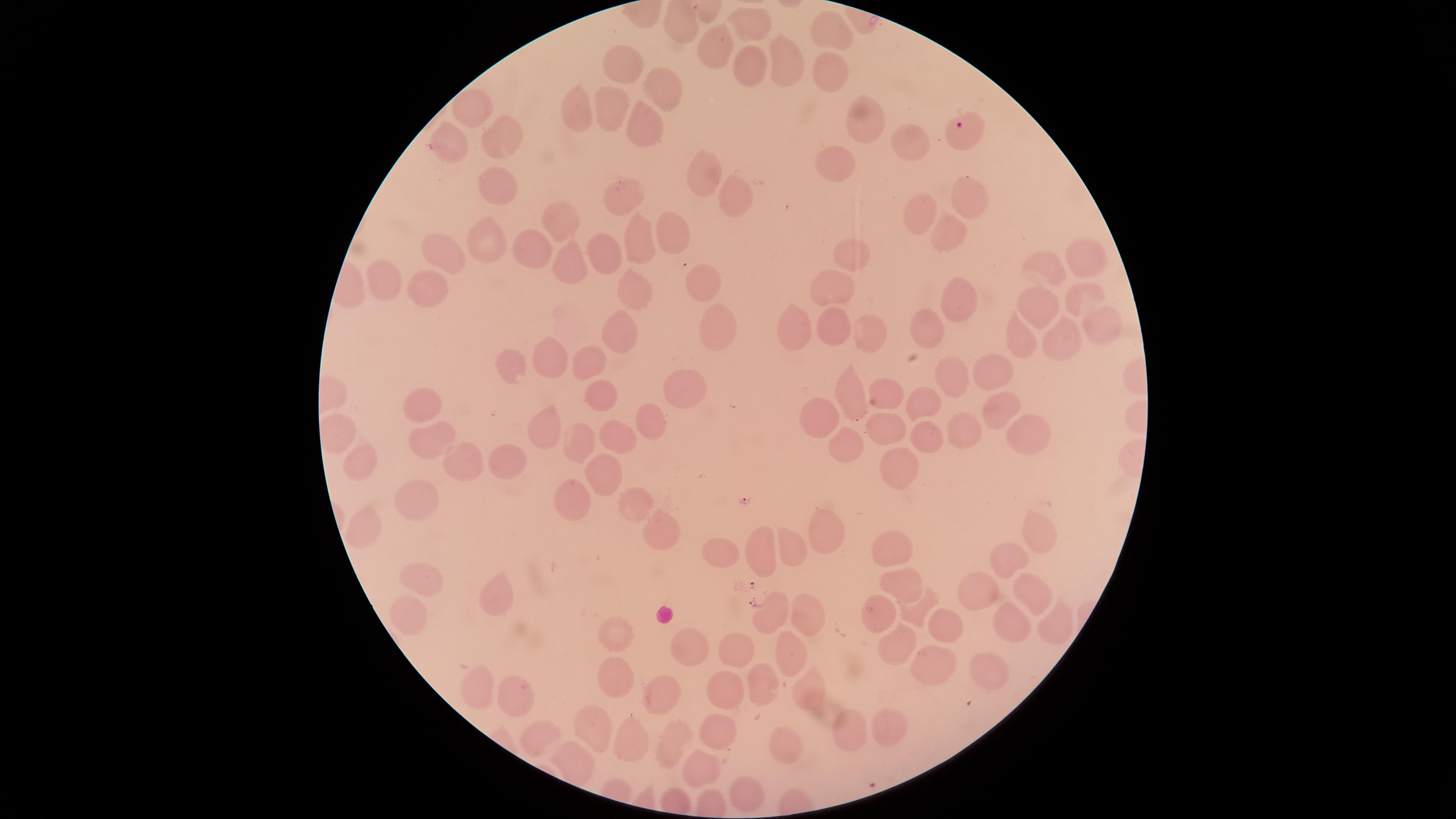
{
  "stain": "Giemsa",
  "uninfected_RBCs": "approximate marker points, in pixels from the top-left corner: (x=752, y=22), (x=676, y=29), (x=836, y=36), (x=716, y=44), (x=784, y=48), (x=628, y=65), (x=747, y=73), (x=833, y=74), (x=670, y=87), (x=574, y=107), (x=608, y=107), (x=470, y=111), (x=866, y=124), (x=643, y=125), (x=501, y=140), (x=446, y=144), (x=911, y=144), (x=839, y=165), (x=702, y=177), (x=495, y=186), (x=731, y=192), (x=631, y=200), (x=968, y=203), (x=922, y=216), (x=558, y=222), (x=670, y=226), (x=952, y=231), (x=486, y=240), (x=640, y=241), (x=534, y=249), (x=607, y=252), (x=442, y=255), (x=1082, y=256), (x=855, y=257), (x=575, y=259), (x=1048, y=273), (x=386, y=283), (x=706, y=286), (x=833, y=287), (x=421, y=292), (x=629, y=295), (x=1079, y=296), (x=970, y=303), (x=1045, y=303), (x=937, y=323), (x=829, y=324), (x=1100, y=324), (x=793, y=325), (x=623, y=328), (x=717, y=330), (x=861, y=330), (x=1024, y=338), (x=1056, y=347), (x=588, y=359), (x=556, y=361), (x=510, y=367), (x=992, y=370), (x=952, y=381), (x=685, y=389), (x=884, y=394), (x=596, y=396), (x=854, y=396), (x=1004, y=400), (x=930, y=401), (x=424, y=409), (x=822, y=414), (x=653, y=421), (x=897, y=425), (x=962, y=431), (x=547, y=434), (x=926, y=434), (x=1027, y=436), (x=619, y=437), (x=431, y=438), (x=581, y=440), (x=843, y=445), (x=360, y=456), (x=499, y=456), (x=465, y=457), (x=898, y=469), (x=602, y=475), (x=412, y=501), (x=564, y=501), (x=630, y=510), (x=363, y=529), (x=655, y=531), (x=1037, y=532), (x=819, y=533), (x=891, y=544), (x=793, y=546), (x=722, y=554), (x=759, y=555), (x=1002, y=560), (x=416, y=584), (x=902, y=585), (x=976, y=591), (x=1026, y=597), (x=494, y=602), (x=879, y=610), (x=410, y=611), (x=910, y=614), (x=801, y=617), (x=767, y=619), (x=1012, y=621), (x=940, y=625), (x=1045, y=628), (x=614, y=631), (x=679, y=645), (x=895, y=647), (x=730, y=653), (x=785, y=654), (x=932, y=665), (x=995, y=668), (x=615, y=684), (x=762, y=685), (x=479, y=686), (x=808, y=690), (x=515, y=692), (x=718, y=692), (x=661, y=699), (x=889, y=725), (x=846, y=730), (x=592, y=731), (x=712, y=731), (x=538, y=736), (x=627, y=738), (x=671, y=747), (x=779, y=749), (x=572, y=761), (x=701, y=766), (x=746, y=792)",
  "parasitized_RBCs": "approximate marker points, in pixels from the top-left corner: (x=962, y=127)",
  "species": "Plasmodium falciparum",
  "visible_region": "circular",
  "image_size": "1456×819 pixels",
  "presence": "malaria parasites seen",
  "capture": "smartphone photograph through the microscope eyepiece",
  "preparation": "thin blood smear",
  "field_of_view": "single"
}